Assess this cell for malaria.
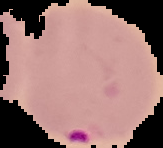
It is parasitized.

Summary:
  - Image type: cell region segmented out of the field of view; surrounding area masked to black
  - Preparation: thin blood film
  - Image size: 163×148 pixels